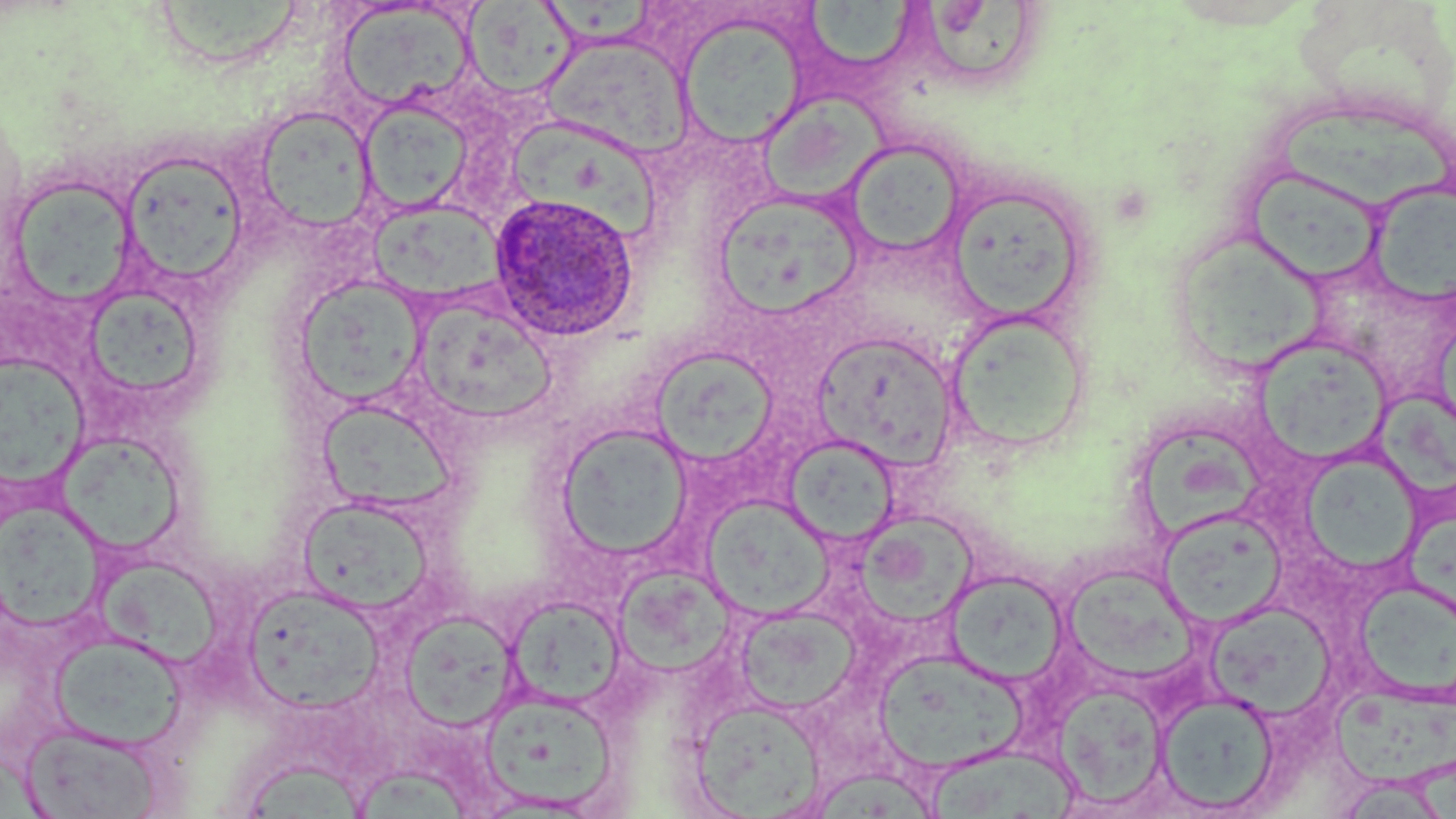

Summary:
  - Coordinate format: approximate bounding boxes as named x1/y1/x2/y2 corners in pixels
  - Uninfected red blood cell locations: (x1=158, y1=0, x2=303, y2=66), (x1=808, y1=0, x2=918, y2=74), (x1=464, y1=2, x2=578, y2=99), (x1=921, y1=2, x2=1034, y2=77), (x1=336, y1=3, x2=477, y2=112), (x1=546, y1=5, x2=656, y2=44), (x1=677, y1=13, x2=809, y2=148), (x1=543, y1=35, x2=692, y2=157), (x1=764, y1=90, x2=890, y2=202), (x1=358, y1=100, x2=472, y2=215), (x1=254, y1=105, x2=375, y2=232), (x1=1280, y1=105, x2=1452, y2=206), (x1=505, y1=120, x2=664, y2=241), (x1=841, y1=139, x2=967, y2=258), (x1=119, y1=150, x2=249, y2=287), (x1=1249, y1=171, x2=1375, y2=282), (x1=5, y1=175, x2=137, y2=306), (x1=1371, y1=183, x2=1456, y2=304), (x1=713, y1=189, x2=865, y2=320), (x1=955, y1=195, x2=1087, y2=322), (x1=366, y1=198, x2=511, y2=300), (x1=1177, y1=231, x2=1327, y2=367), (x1=294, y1=276, x2=427, y2=407), (x1=88, y1=287, x2=206, y2=397), (x1=412, y1=303, x2=562, y2=419), (x1=945, y1=307, x2=1091, y2=453), (x1=1428, y1=328, x2=1456, y2=414), (x1=812, y1=330, x2=958, y2=470), (x1=1258, y1=337, x2=1394, y2=466), (x1=649, y1=345, x2=780, y2=465), (x1=0, y1=354, x2=89, y2=490), (x1=1380, y1=392, x2=1456, y2=495), (x1=317, y1=398, x2=457, y2=514), (x1=554, y1=422, x2=694, y2=561), (x1=1141, y1=426, x2=1263, y2=538), (x1=58, y1=435, x2=180, y2=552), (x1=785, y1=435, x2=899, y2=546), (x1=1304, y1=462, x2=1424, y2=573), (x1=297, y1=497, x2=436, y2=616), (x1=702, y1=497, x2=832, y2=617), (x1=0, y1=502, x2=107, y2=632), (x1=854, y1=511, x2=981, y2=627), (x1=1159, y1=511, x2=1286, y2=626), (x1=1404, y1=514, x2=1456, y2=615), (x1=100, y1=565, x2=231, y2=668), (x1=613, y1=565, x2=739, y2=686), (x1=945, y1=569, x2=1070, y2=686), (x1=1064, y1=569, x2=1190, y2=679), (x1=1357, y1=582, x2=1456, y2=698), (x1=242, y1=584, x2=386, y2=713), (x1=506, y1=595, x2=628, y2=711), (x1=1206, y1=600, x2=1337, y2=718), (x1=734, y1=606, x2=859, y2=714), (x1=399, y1=609, x2=521, y2=731), (x1=49, y1=632, x2=188, y2=751), (x1=873, y1=649, x2=1026, y2=774), (x1=1053, y1=682, x2=1168, y2=809), (x1=479, y1=688, x2=620, y2=811), (x1=1331, y1=690, x2=1456, y2=785), (x1=1156, y1=692, x2=1280, y2=814), (x1=691, y1=697, x2=825, y2=816), (x1=19, y1=722, x2=165, y2=819), (x1=928, y1=741, x2=1082, y2=819), (x1=245, y1=761, x2=363, y2=819), (x1=359, y1=766, x2=475, y2=819), (x1=814, y1=769, x2=937, y2=819), (x1=1330, y1=775, x2=1455, y2=818)
  - Plasmodium ovale-infected red blood cell locations: (x1=488, y1=191, x2=641, y2=341)
  - Slide-level diagnosis: Plasmodium ovale
  - Stain: May-Grünwald-Giemsa
  - Field of view: one of a larger specimen
  - Image size: 1456×819 pixels
  - Preparation: thin blood smear
  - Modality: optical microscopy
  - Magnification: 1000x